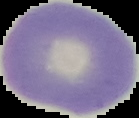

image size = 139×118 pixels
image type = cell region segmented out of the field of view; surrounding area masked to black
malaria status = uninfected
preparation = thin blood smear